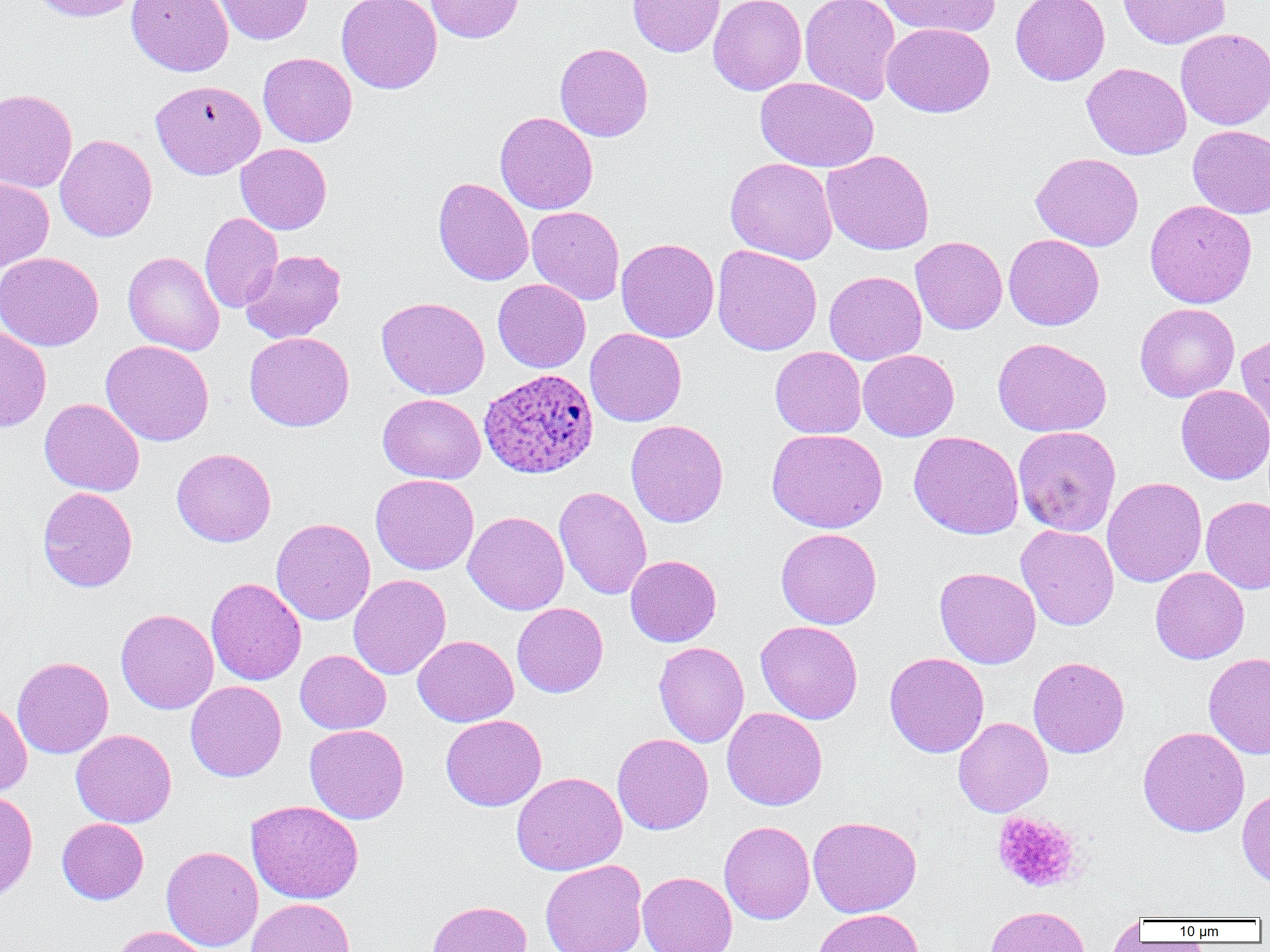

slide-level diagnosis = Plasmodium ovale
platelet locations = approximate bounding boxes as (x1, y1, x2, y2) in pixels: (991, 811, 1084, 893)
preparation = thin blood film
modality = optical microscopy
field of view = single
magnification = 1000x
uninfected red blood cell locations = approximate bounding boxes as (x1, y1, x2, y2) in pixels: (28, 0, 142, 22), (126, 0, 234, 77), (214, 0, 314, 45), (336, 0, 442, 94), (425, 0, 524, 43), (627, 0, 725, 57), (708, 0, 807, 95), (799, 0, 901, 105), (879, 0, 1000, 38), (1010, 0, 1110, 86), (1117, 0, 1231, 49), (882, 22, 995, 117), (1176, 28, 1270, 130), (554, 42, 653, 142), (258, 52, 357, 147), (1082, 62, 1191, 159), (755, 77, 878, 172), (150, 79, 265, 179), (0, 89, 77, 193), (495, 112, 598, 215), (1188, 125, 1270, 218), (55, 134, 157, 242), (235, 143, 331, 234), (822, 150, 935, 255), (1030, 152, 1143, 251), (725, 157, 838, 264), (0, 177, 54, 271), (433, 177, 534, 286), (1145, 200, 1257, 308), (527, 206, 625, 305), (200, 212, 282, 313), (1004, 234, 1104, 330), (910, 236, 1008, 334), (616, 238, 719, 343), (712, 245, 822, 356), (240, 249, 346, 343), (123, 251, 225, 355), (0, 252, 103, 351), (824, 270, 927, 365), (493, 279, 591, 373), (376, 297, 490, 400), (1134, 303, 1240, 402), (0, 327, 52, 432), (585, 328, 687, 426), (1235, 330, 1270, 438), (244, 332, 354, 431), (992, 337, 1111, 437), (101, 340, 214, 446), (770, 346, 866, 438), (858, 349, 959, 441), (1175, 384, 1270, 485), (378, 394, 486, 483), (39, 398, 144, 496), (625, 420, 729, 527), (1013, 426, 1121, 536), (767, 428, 888, 533), (908, 431, 1024, 540), (171, 448, 276, 547), (370, 474, 479, 575), (1102, 476, 1207, 588), (553, 486, 652, 600), (37, 487, 138, 592), (1201, 496, 1270, 594), (463, 511, 569, 615), (271, 518, 376, 625), (1016, 524, 1119, 631), (775, 527, 882, 629), (625, 555, 722, 647), (1150, 566, 1250, 664), (934, 567, 1041, 669), (348, 574, 451, 680), (206, 577, 306, 685), (512, 603, 608, 697), (116, 608, 218, 714), (755, 620, 863, 724), (412, 635, 518, 727), (654, 642, 749, 748), (295, 650, 391, 734), (884, 652, 989, 758), (1203, 652, 1270, 759), (12, 656, 114, 758), (1027, 656, 1130, 758), (185, 680, 287, 782), (0, 700, 32, 797), (722, 707, 828, 811), (440, 714, 547, 811), (953, 717, 1053, 817), (304, 724, 409, 824), (1138, 726, 1250, 837), (71, 729, 177, 828), (612, 733, 713, 835), (511, 772, 627, 875), (1236, 787, 1270, 889), (0, 790, 38, 903), (246, 799, 363, 904), (808, 816, 922, 918), (57, 818, 149, 904), (719, 821, 815, 924), (161, 846, 263, 951), (540, 859, 648, 952), (637, 872, 738, 952), (245, 898, 356, 952), (426, 899, 532, 952), (985, 905, 1091, 952), (813, 908, 925, 952), (1107, 913, 1144, 951), (112, 925, 213, 952)
image size = 1270×952 pixels
Plasmodium ovale-infected red blood cell locations = approximate bounding boxes as (x1, y1, x2, y2) in pixels: (479, 369, 599, 479)